State which parasite is depicted.
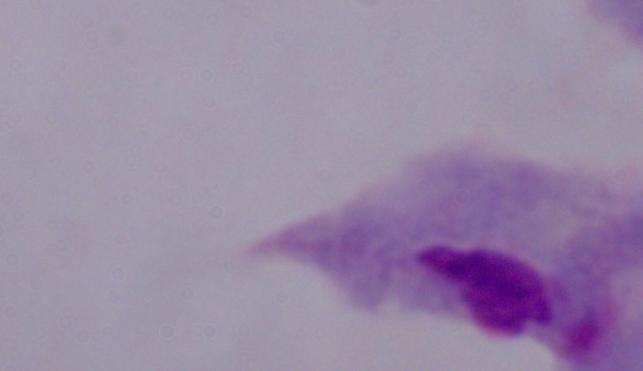

This is a trichomonad.

magnification = 1000x
modality = micrograph